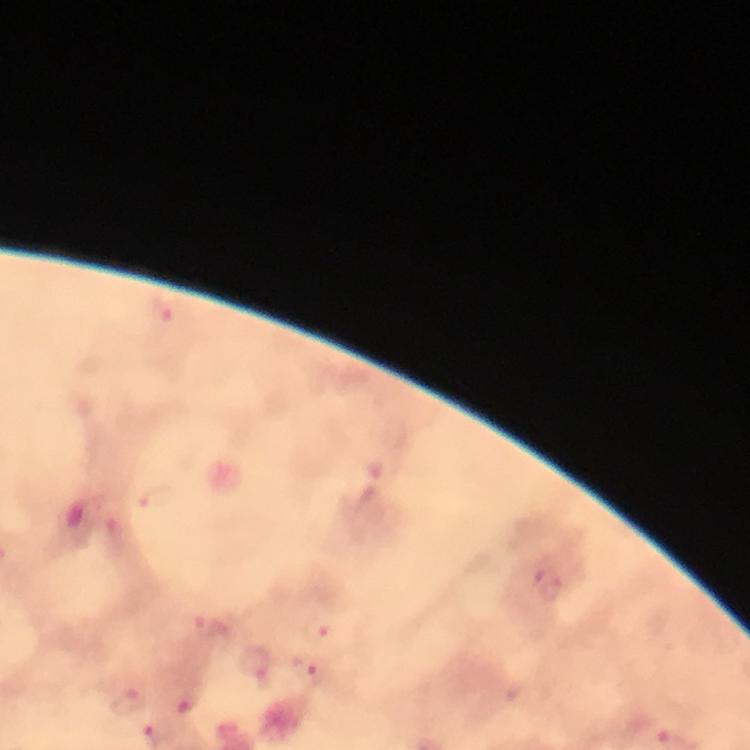

Approximate centers as (x, y) in pixels. Plasmodium parasite locations: (163, 310), (547, 583), (319, 628), (254, 666), (310, 672). From a malaria diagnostic workup. Thick blood film. Image is 750×750 pixels. Giemsa stain. At 100x magnification. Immersion oil was used. A crop from one field of view. Photographed through the microscope with a smartphone camera.